Give the position of every malaria parasite.
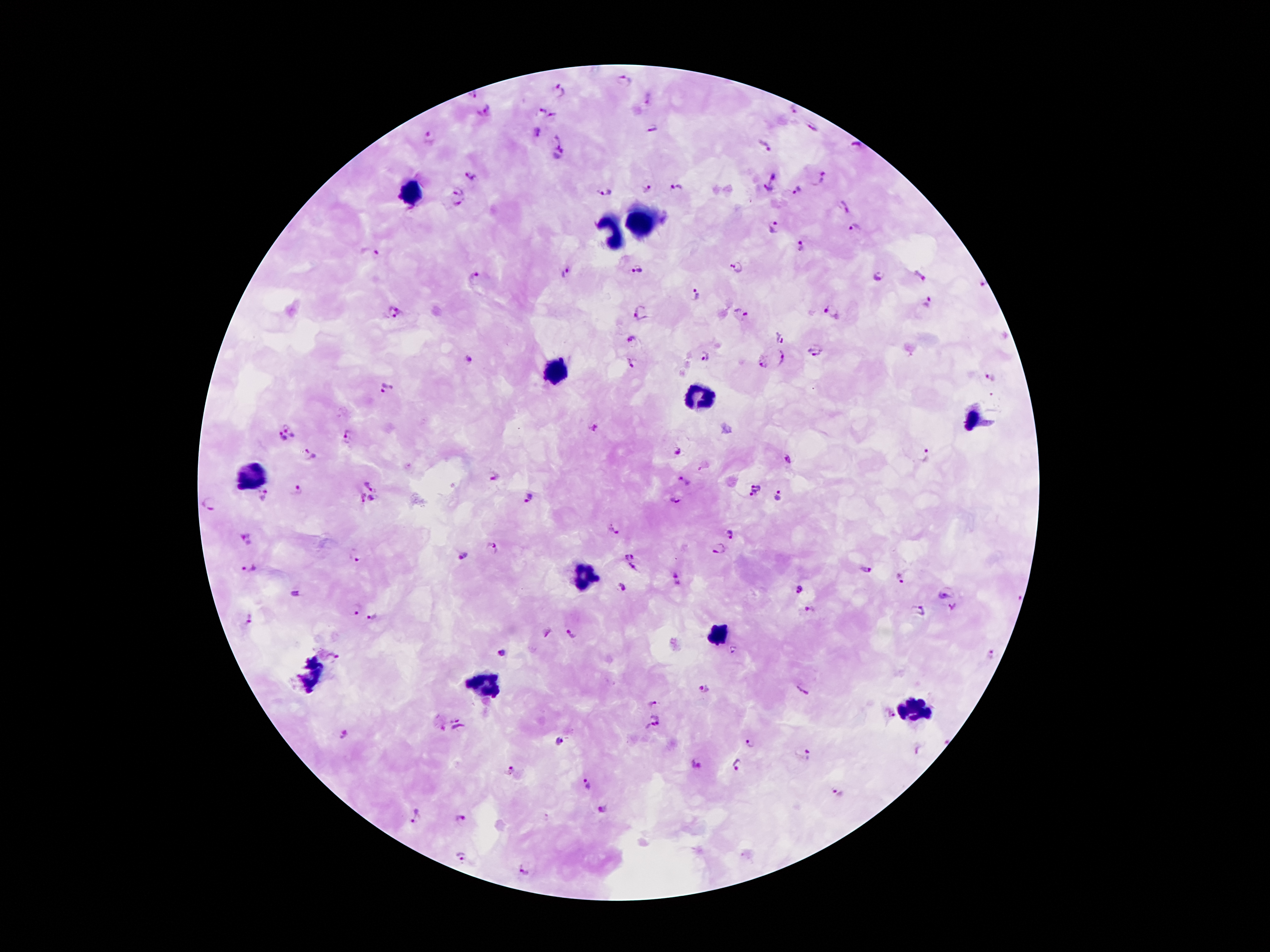

Approximate centers as {x, y} in pixels.
Malaria parasites: {623, 81}, {560, 91}, {474, 95}, {542, 109}, {795, 109}, {485, 112}, {551, 115}, {813, 126}, {652, 129}, {538, 132}, {428, 136}, {553, 141}, {856, 144}, {763, 146}, {561, 156}, {469, 175}, {773, 177}, {818, 179}, {646, 189}, {676, 189}, {766, 189}, {797, 190}, {458, 191}, {603, 192}, {458, 205}, {844, 208}, {774, 225}, {856, 228}, {802, 246}, {375, 253}, {735, 265}, {637, 267}, {567, 272}, {919, 276}, {879, 277}, {475, 278}, {985, 286}, {696, 293}, {929, 303}, {832, 310}, {641, 311}, {393, 312}, {741, 315}, {780, 338}, {634, 340}, {815, 350}, {705, 356}, {783, 359}, {469, 361}, {763, 363}, {631, 365}, {992, 378}, {386, 388}, {291, 427}, {595, 429}, {348, 437}, {281, 439}, {680, 451}, {928, 454}, {308, 455}, {789, 458}, {494, 476}, {686, 480}, {373, 484}, {756, 490}, {299, 491}, {261, 494}, {780, 495}, {358, 498}, {529, 499}, {677, 499}, {373, 501}, {210, 505}, {614, 530}, {730, 533}, {246, 539}, {491, 548}, {718, 549}, {630, 554}, {463, 555}, {355, 556}, {252, 567}, {634, 567}, {866, 570}, {678, 577}, {901, 578}, {622, 586}, {802, 591}, {296, 593}, {947, 594}, {954, 607}, {353, 610}, {809, 610}, {920, 610}, {371, 617}, {248, 619}, {550, 633}, {572, 633}, {500, 652}, {991, 654}, {339, 655}, {704, 689}, {802, 690}, {653, 705}, {889, 716}, {654, 723}, {458, 728}, {344, 734}, {559, 743}, {751, 743}, {807, 755}, {695, 763}, {737, 767}, {510, 771}, {587, 783}, {837, 794}, {603, 810}, {460, 814}, {417, 816}, {461, 856}, {523, 869}.

Summary:
  - Leukocyte locations: {414, 195}, {640, 223}, {608, 235}, {556, 368}, {700, 395}, {974, 420}, {250, 475}, {584, 575}, {720, 634}, {312, 674}, {488, 684}, {916, 712}
  - Magnification: 100x
  - Image size: 1270×952 pixels
  - Preparation: thick blood film
  - Field of view: one from this slide
  - Stain: Giemsa
  - Patient malaria status: infected with Plasmodium falciparum
  - Capture: smartphone through the microscope eyepiece